Assess for malaria.
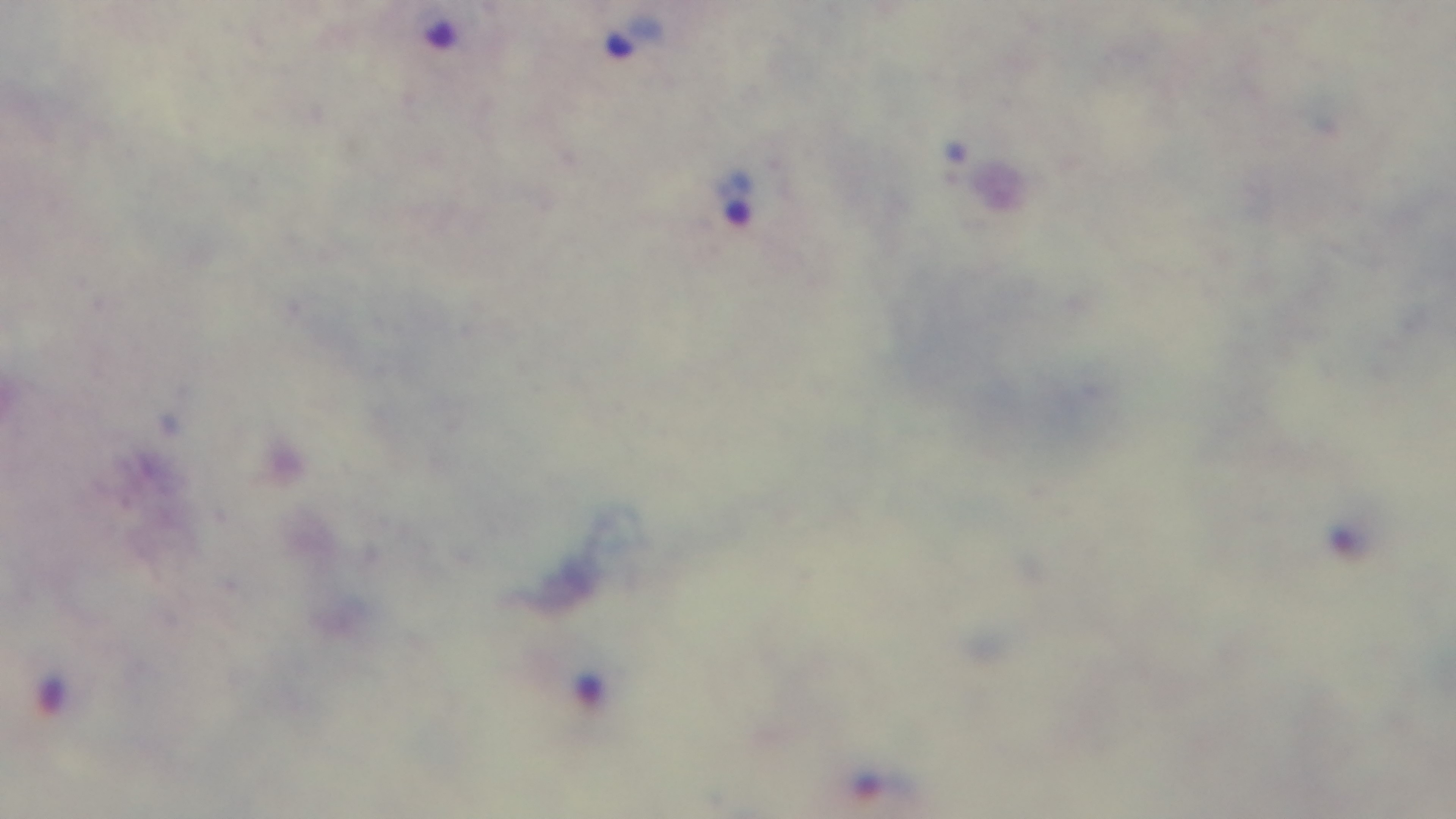
It is infected.

Giemsa-stained. One field from the slide. 100x oil-immersion objective. Light microscopy. Preparation: thick blood film. Captured with a mounted 4K digital camera.